Assess the morphology of the erythrocytes.
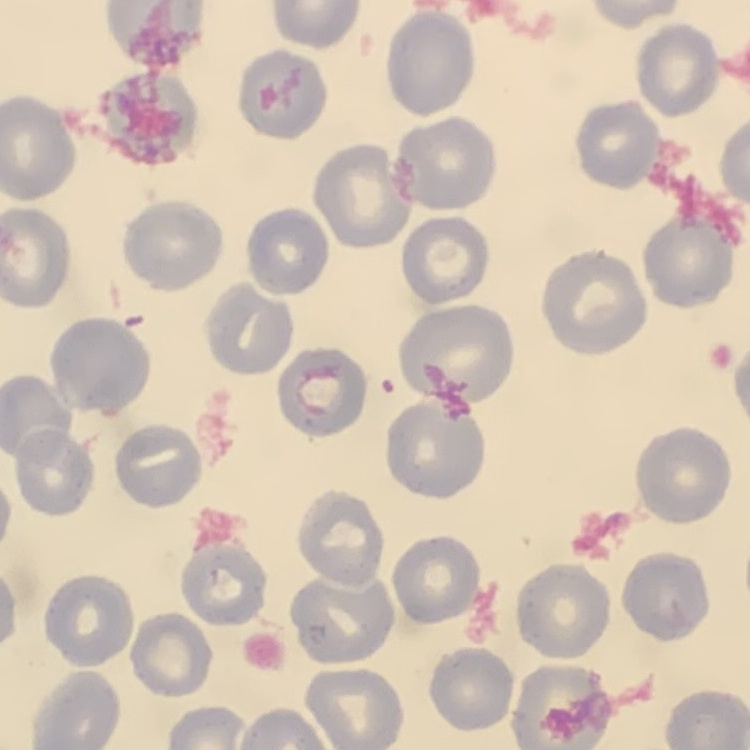

No rouleaux formation.

{
  "image_type": "one tile cut from a larger photomicrograph",
  "stain": "Field's or Giemsa",
  "preparation": "thin blood smear"
}